Describe the morphology of the erythrocytes.
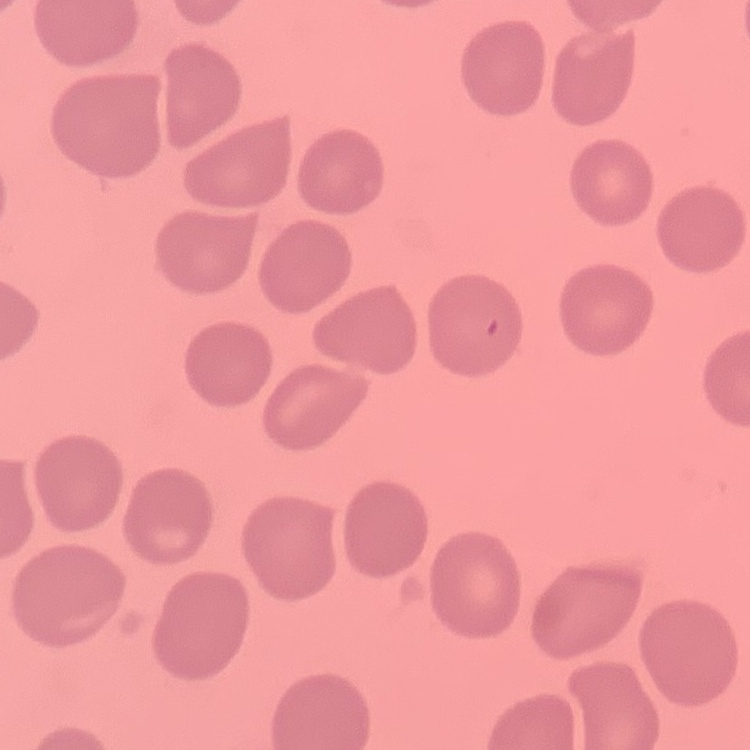

No rouleaux formation.

stain: Field's or Giemsa
image_type: one tile cut from a larger photomicrograph
preparation: thin peripheral smear